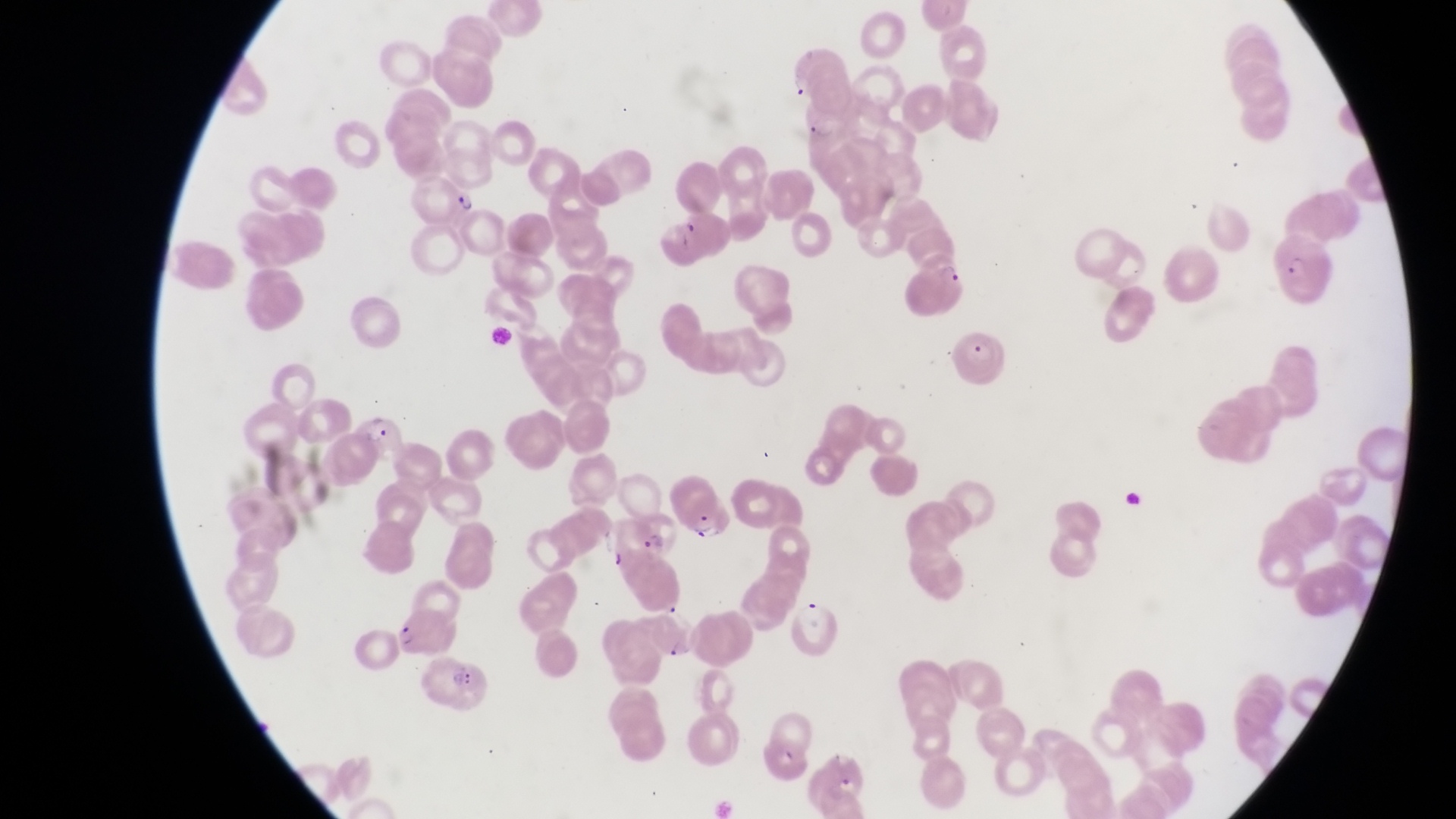

Approximate bounding boxes as {left, top, right, bottom} in pixels. Trophozoite locations: {450, 185, 480, 217}. Parasitised red blood cell locations: {802, 112, 845, 149}, {1269, 234, 1330, 307}, {951, 325, 1012, 388}, {351, 412, 409, 473}, {674, 486, 726, 541}, {629, 507, 688, 565}, {645, 601, 704, 662}, {389, 608, 456, 658}, {420, 653, 492, 712}. Thin blood smear. Single field of view. Image is 1456×819 pixels. At a magnification of 1000x. Collected in Uganda. Photographed through the eyepiece of an Olympus CX-23 microscope with a smartphone camera.